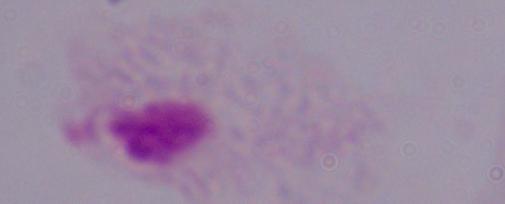

1000x magnification. A trichomonad is shown. Micrograph.